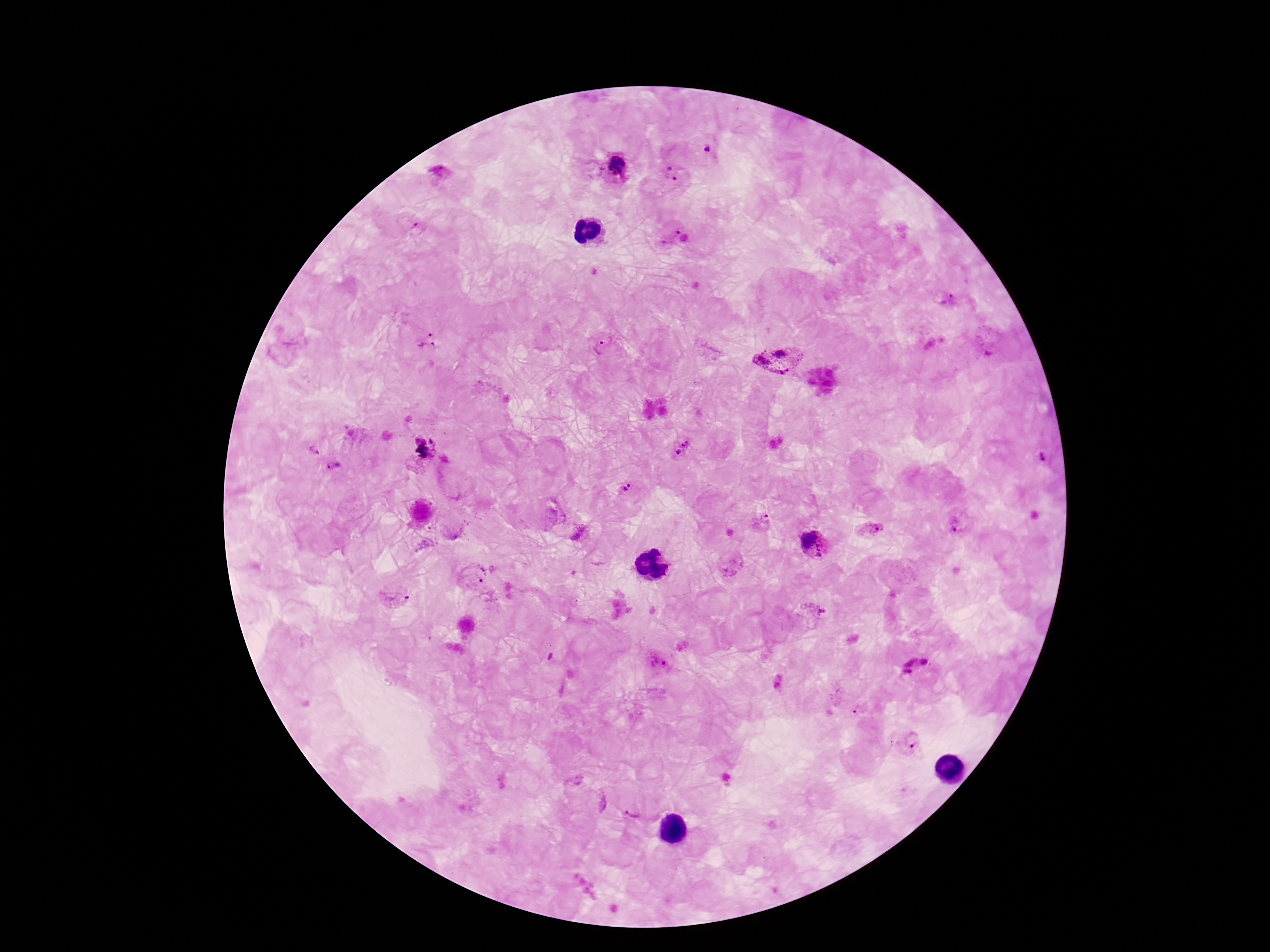

Approximate centers as (x, y) in pixels.
Summary:
  - Plasmodium parasite locations: (707, 147), (617, 167), (441, 173), (676, 173), (417, 224), (675, 238), (946, 301), (427, 342), (604, 346), (780, 358), (681, 449), (313, 450), (1042, 458), (334, 467), (625, 488), (761, 522), (958, 524), (867, 529), (580, 534), (815, 546), (474, 574), (395, 598), (655, 663), (914, 666), (778, 682), (861, 710), (909, 740), (632, 816)
  - Image size: 1270×952 pixels
  - Stain: Giemsa
  - Magnification: 100x
  - Patient malaria status: infected
  - Preparation: thick peripheral-blood smear
  - Field of view: one from this slide
  - Capture: smartphone camera through the microscope eyepiece